Identify the parasite.
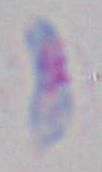

This is Toxoplasma gondii.

magnification: 1000x
modality: micrograph